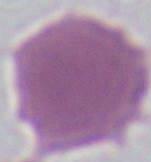
Micrograph. A red blood cell is shown. 1000x magnification.